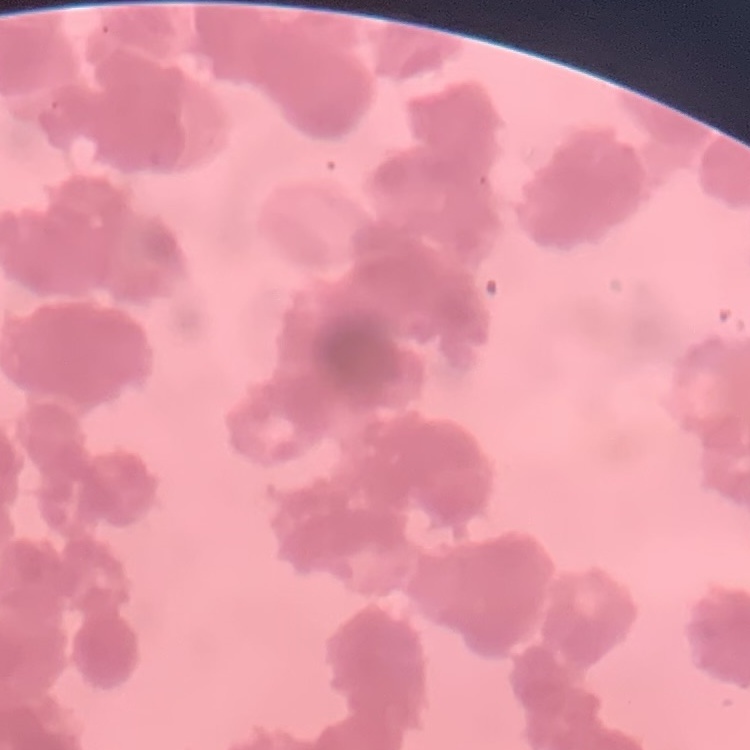

red blood cell morphology = rouleaux formation
image type = square crop of a larger photomicrograph
preparation = thin peripheral smear
stain = Field's or Giemsa